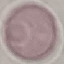 Malaria status: uninfected. Giemsa stain. Thin blood film. Automatically extracted cell patch, resized to 64 × 64 pixels. Photographed with a smartphone camera at the microscope eyepiece.